Describe the morphology of the erythrocytes.
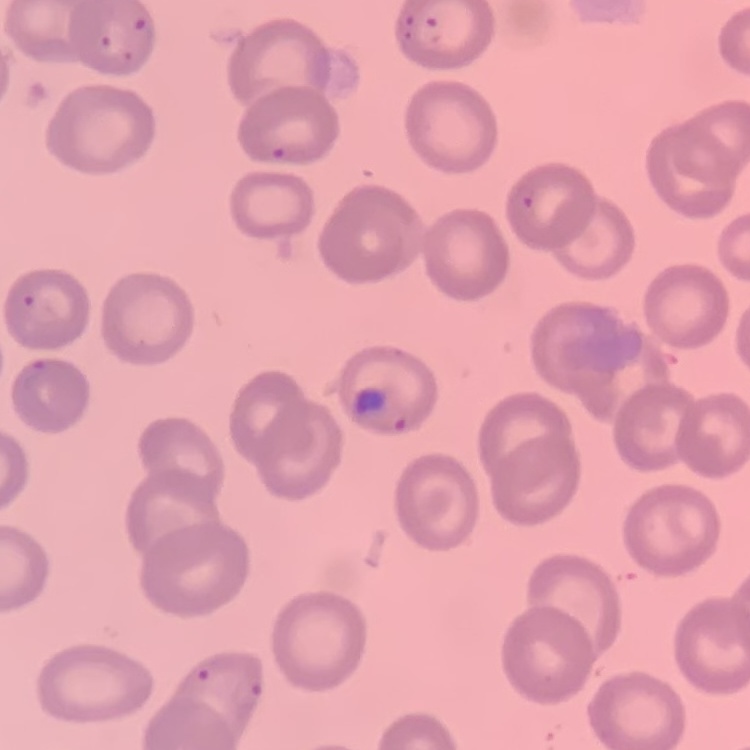
They show no rouleaux formation.

image type = square crop of a larger photomicrograph
stain = Field's or Giemsa
preparation = thin blood smear